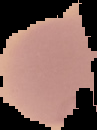
Summary:
  - Image type: cell region segmented out of the field of view; surrounding area masked to black
  - Result: Plasmodium parasites detected
  - Preparation: thin blood smear
  - Image size: 97×130 pixels